Classify this cell by malaria status.
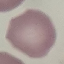

It is uninfected.

image type = cell patch, automatically extracted from a larger field of view and resized to 64 × 64 pixels
preparation = thin blood smear
capture = smartphone through the microscope eyepiece
stain = Giemsa